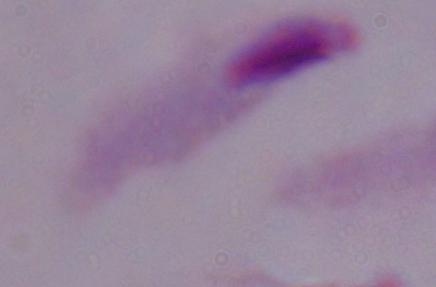

Summary:
  - Magnification: 1000x
  - Identification: trichomonad
  - Modality: photomicrograph